Assess the morphology of the erythrocytes.
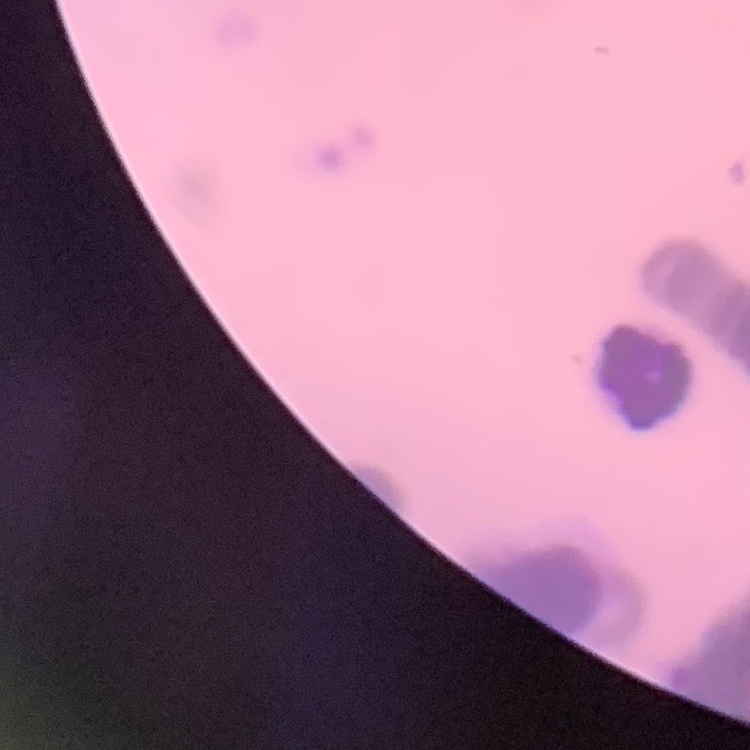
They show rouleaux formation.

{
  "preparation": "thin blood film",
  "image_type": "square crop of a larger photomicrograph",
  "stain": "Field's or Giemsa"
}